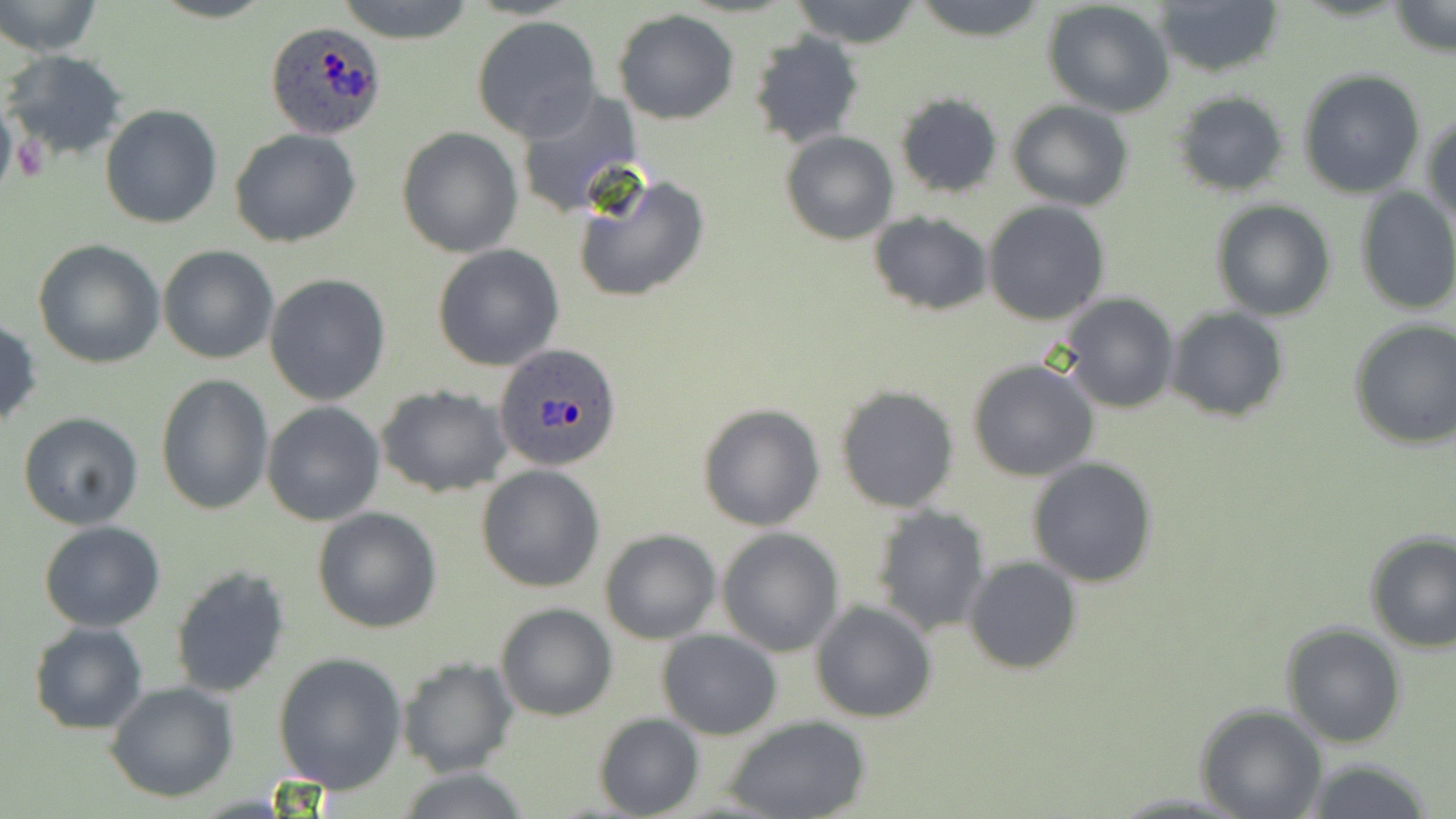
Summary:
  - Coordinate format: approximate bounding boxes as named x1/y1/x2/y2 corners in pixels
  - Uninfected red blood cell locations: (x1=1, y1=0, x2=104, y2=57), (x1=333, y1=0, x2=481, y2=45), (x1=788, y1=0, x2=925, y2=48), (x1=909, y1=0, x2=1050, y2=39), (x1=1153, y1=0, x2=1286, y2=77), (x1=1043, y1=2, x2=1175, y2=117), (x1=1389, y1=2, x2=1453, y2=57), (x1=614, y1=9, x2=739, y2=124), (x1=473, y1=17, x2=602, y2=141), (x1=746, y1=32, x2=866, y2=151), (x1=763, y1=35, x2=882, y2=247), (x1=1, y1=48, x2=130, y2=163), (x1=1297, y1=68, x2=1426, y2=198), (x1=512, y1=90, x2=644, y2=218), (x1=1170, y1=90, x2=1292, y2=197), (x1=895, y1=94, x2=1002, y2=199), (x1=1007, y1=100, x2=1134, y2=210), (x1=100, y1=103, x2=222, y2=229), (x1=1423, y1=109, x2=1456, y2=230), (x1=229, y1=127, x2=362, y2=248), (x1=396, y1=127, x2=522, y2=257), (x1=779, y1=129, x2=899, y2=245), (x1=571, y1=170, x2=713, y2=303), (x1=1354, y1=187, x2=1456, y2=315), (x1=1209, y1=199, x2=1336, y2=322), (x1=983, y1=200, x2=1110, y2=326), (x1=868, y1=210, x2=991, y2=316), (x1=32, y1=239, x2=164, y2=369), (x1=158, y1=244, x2=280, y2=364), (x1=432, y1=246, x2=564, y2=370), (x1=265, y1=273, x2=391, y2=406), (x1=1060, y1=293, x2=1180, y2=413), (x1=1165, y1=307, x2=1289, y2=424), (x1=0, y1=317, x2=43, y2=433), (x1=1347, y1=319, x2=1455, y2=451), (x1=965, y1=357, x2=1099, y2=482), (x1=155, y1=372, x2=274, y2=514), (x1=834, y1=384, x2=960, y2=513), (x1=377, y1=385, x2=512, y2=496), (x1=262, y1=400, x2=385, y2=525), (x1=697, y1=403, x2=825, y2=531), (x1=17, y1=412, x2=144, y2=529), (x1=1026, y1=457, x2=1159, y2=587), (x1=476, y1=464, x2=605, y2=593), (x1=870, y1=504, x2=992, y2=638), (x1=312, y1=507, x2=442, y2=632), (x1=39, y1=521, x2=166, y2=632), (x1=717, y1=528, x2=844, y2=656), (x1=600, y1=529, x2=721, y2=644), (x1=1363, y1=532, x2=1456, y2=654), (x1=964, y1=557, x2=1081, y2=674), (x1=170, y1=565, x2=289, y2=698), (x1=810, y1=599, x2=937, y2=725), (x1=495, y1=602, x2=619, y2=720), (x1=28, y1=622, x2=149, y2=734), (x1=1279, y1=623, x2=1406, y2=749), (x1=657, y1=630, x2=783, y2=740), (x1=69, y1=651, x2=213, y2=782), (x1=273, y1=653, x2=408, y2=794), (x1=396, y1=655, x2=516, y2=780), (x1=105, y1=681, x2=239, y2=803), (x1=1196, y1=705, x2=1327, y2=819), (x1=593, y1=711, x2=703, y2=819), (x1=722, y1=715, x2=872, y2=819), (x1=1293, y1=760, x2=1436, y2=818), (x1=390, y1=768, x2=534, y2=819)
  - Platelet locations: (x1=14, y1=134, x2=51, y2=183)
  - Plasmodium ovale-infected red blood cell locations: (x1=263, y1=19, x2=390, y2=141), (x1=494, y1=343, x2=624, y2=472)
  - Slide-level diagnosis: Plasmodium ovale
  - Image size: 1456×819 pixels
  - Preparation: thin blood smear
  - Stain: May-Grünwald-Giemsa
  - Field of view: one of a larger specimen
  - Magnification: 1000x
  - Modality: light microscopy